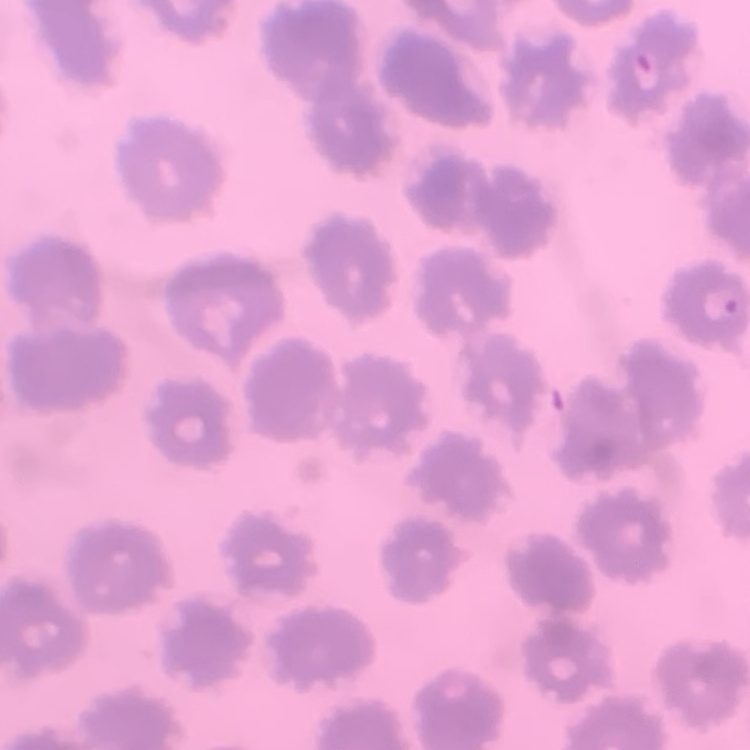

Summary:
  - Erythrocyte morphology: no rouleaux formation
  - Image type: square crop of a larger photomicrograph
  - Preparation: thin blood smear
  - Stain: Field's or Giemsa